Report the malaria status of this cell.
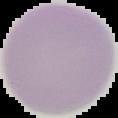
Uninfected.

Summary:
  - Preparation: thin blood smear
  - Image type: segmented cell region on a black background
  - Image size: 118×118 pixels